Classify this cell by malaria status.
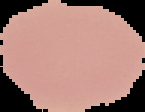
It is uninfected.

Cell region segmented out of the field of view; the surrounding area is masked to black. From a thin blood film. Image is 145×112 pixels.